Classify this cell by malaria status.
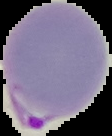

It is parasitized.

Summary:
  - Preparation: thin blood smear
  - Image type: segmented cell region with the area outside set to black
  - Image size: 112×136 pixels